Comment on the morphology of the red blood cells.
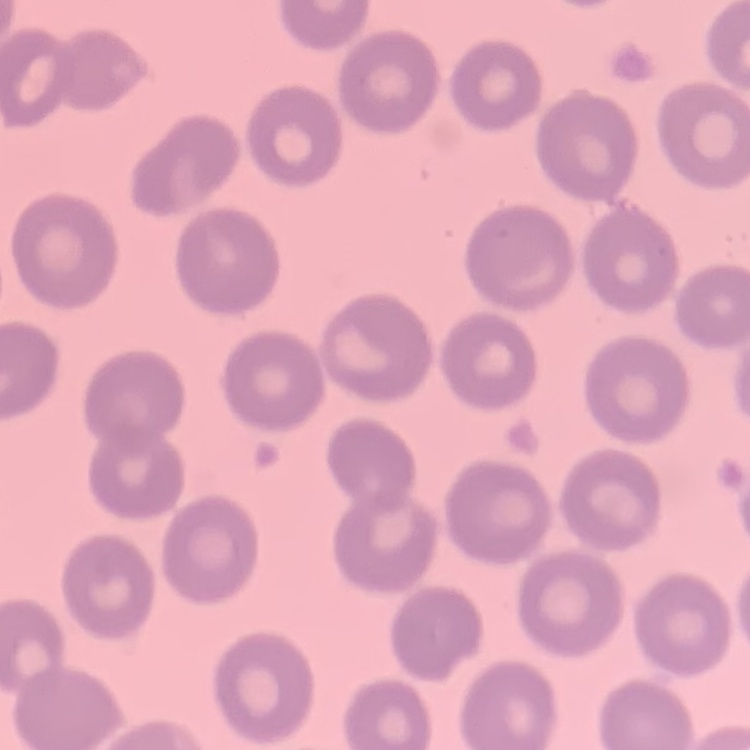
No rouleaux formation.

One tile cut from a larger photomicrograph. Thin blood film. Field's or Giemsa stain.